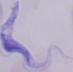
A trypanosome is seen. Micrograph. 1000x magnification.